Report the malaria status of this cell.
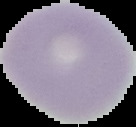
Uninfected.

{
  "preparation": "thin blood film",
  "image_size": "136×127 pixels",
  "image_type": "segmented cell region with the area outside set to black"
}